Locate and identify every blood parasite.
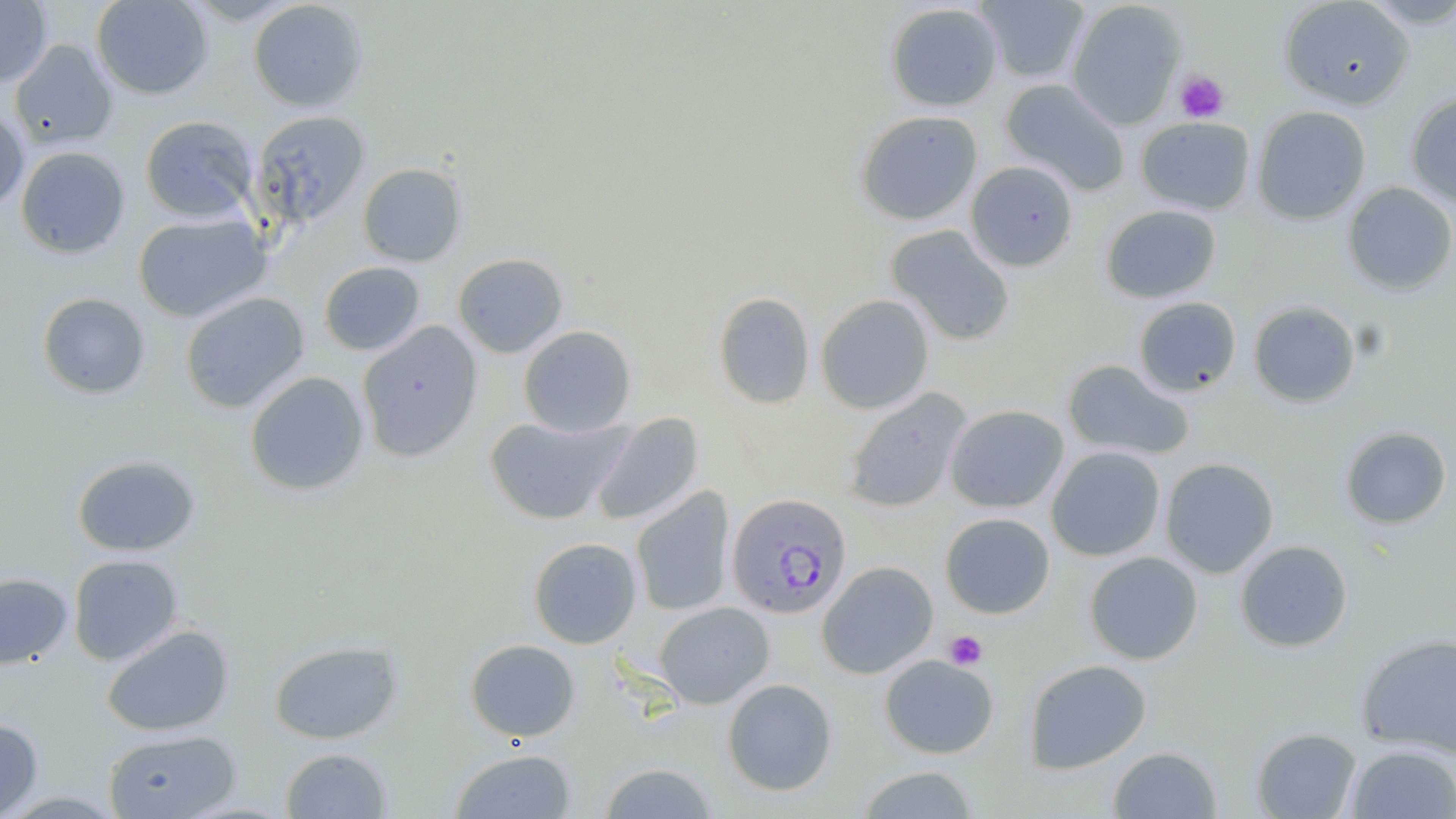
Approximate bounding boxes as (x1, y1, x2, y2) in pixels.
Plasmodium falciparum-infected red blood cells: (727, 493, 852, 618).
No Plasmodium ovale, Plasmodium malariae, Plasmodium vivax, Babesia divergens, or Trypanosoma brucei observed.

Summary:
  - Uninfected red blood cell locations: (0, 0, 53, 88), (91, 0, 214, 99), (976, 0, 1090, 84), (1279, 0, 1415, 110), (1358, 0, 1456, 28), (248, 1, 369, 113), (1065, 1, 1187, 130), (885, 3, 1003, 112), (10, 40, 118, 150), (999, 78, 1130, 196), (1405, 93, 1456, 207), (0, 105, 29, 215), (1252, 106, 1371, 224), (855, 110, 983, 225), (250, 111, 370, 229), (140, 115, 259, 224), (1136, 117, 1255, 214), (15, 146, 130, 258), (965, 161, 1079, 271), (357, 163, 467, 267), (1341, 182, 1456, 296), (1101, 204, 1222, 303), (133, 213, 271, 323), (885, 225, 1016, 346), (453, 253, 568, 358), (319, 261, 426, 356), (713, 291, 815, 409), (37, 292, 151, 399), (180, 292, 309, 413), (816, 295, 934, 413), (1133, 296, 1241, 397), (1248, 301, 1361, 407), (357, 321, 483, 461), (519, 325, 636, 437), (1062, 359, 1194, 460), (245, 371, 369, 496), (843, 388, 971, 513), (945, 404, 1069, 513), (591, 413, 704, 526), (484, 415, 629, 525), (1339, 426, 1452, 529), (1046, 446, 1166, 561), (71, 454, 201, 556), (1159, 457, 1279, 578), (631, 487, 735, 617), (940, 512, 1055, 619), (528, 537, 642, 648), (1234, 540, 1353, 652), (1084, 551, 1203, 665), (68, 554, 184, 665), (817, 561, 938, 678), (0, 573, 73, 669), (654, 601, 774, 708), (101, 624, 234, 737), (1356, 633, 1456, 758), (465, 638, 580, 741), (269, 640, 403, 744), (879, 655, 999, 758), (1024, 659, 1151, 774), (722, 678, 837, 796), (0, 718, 43, 818), (1251, 727, 1362, 818), (104, 729, 241, 818), (1345, 745, 1456, 818), (1108, 746, 1223, 818), (280, 747, 393, 818), (450, 749, 577, 818), (599, 762, 718, 819), (855, 765, 981, 819)
  - Platelet locations: (1174, 70, 1230, 123), (944, 630, 987, 670)
  - Slide-level diagnosis: Plasmodium falciparum
  - Image size: 1456×819 pixels
  - Magnification: 1000x
  - Stain: May-Grünwald-Giemsa
  - Modality: light microscopy
  - Preparation: thin blood smear
  - Field of view: one of a larger specimen